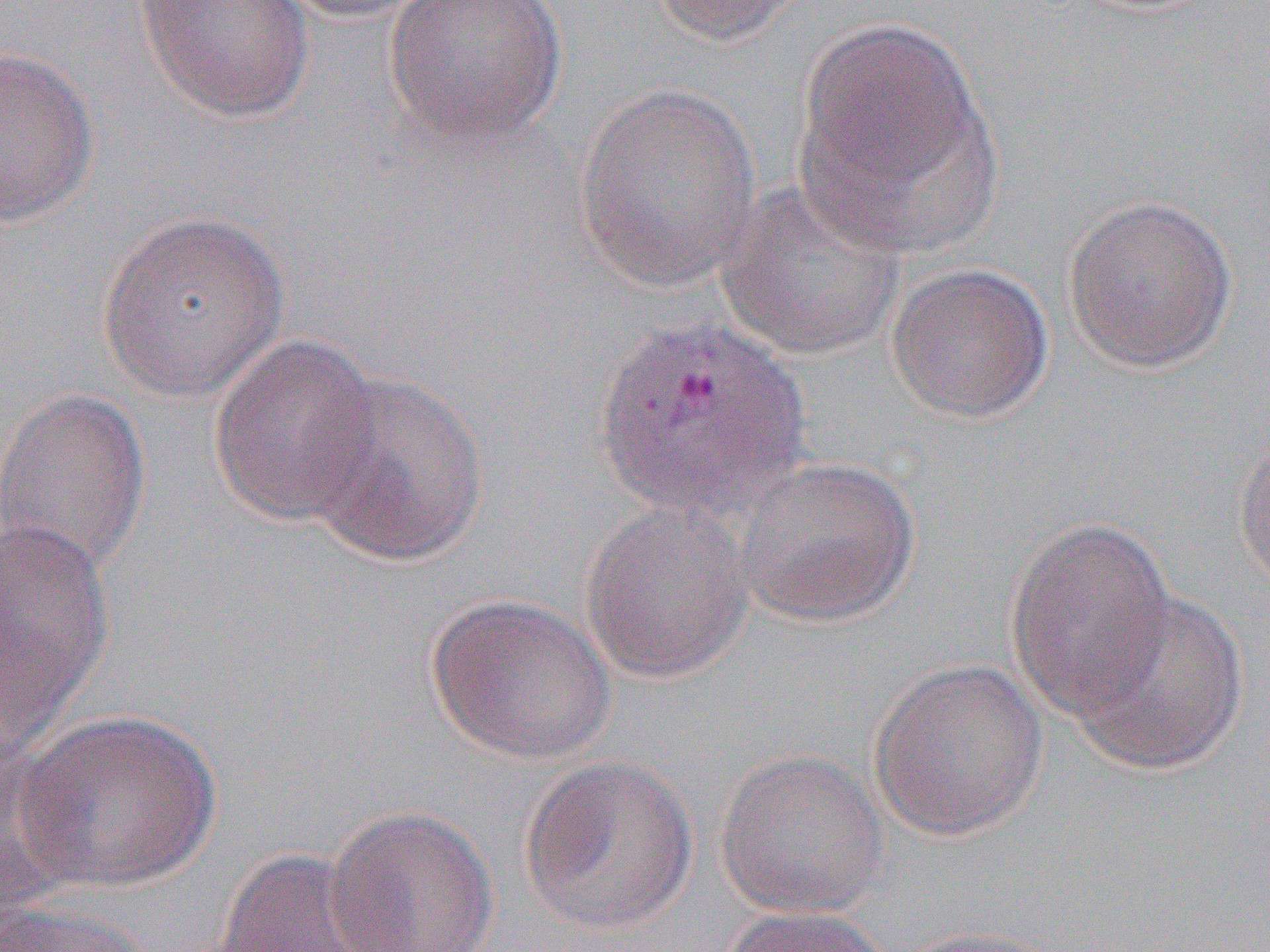
Summary:
  - Coordinate format: approximate bounding boxes as named x1/y1/x2/y2 corners in pixels
  - Uninfected red blood cell locations: (x1=133, y1=0, x2=316, y2=124), (x1=271, y1=0, x2=439, y2=24), (x1=381, y1=0, x2=568, y2=151), (x1=645, y1=0, x2=808, y2=48), (x1=792, y1=17, x2=1002, y2=254), (x1=0, y1=46, x2=100, y2=228), (x1=573, y1=81, x2=762, y2=294), (x1=714, y1=179, x2=909, y2=363), (x1=1061, y1=193, x2=1238, y2=376), (x1=96, y1=208, x2=292, y2=403), (x1=885, y1=262, x2=1055, y2=425), (x1=208, y1=332, x2=387, y2=528), (x1=300, y1=370, x2=492, y2=569), (x1=1, y1=385, x2=152, y2=579), (x1=1232, y1=423, x2=1270, y2=593), (x1=729, y1=453, x2=920, y2=628), (x1=579, y1=499, x2=755, y2=684), (x1=0, y1=513, x2=115, y2=740), (x1=1005, y1=515, x2=1177, y2=720), (x1=1064, y1=589, x2=1251, y2=777), (x1=425, y1=593, x2=618, y2=765), (x1=868, y1=657, x2=1050, y2=842), (x1=12, y1=709, x2=224, y2=894), (x1=0, y1=741, x2=81, y2=921), (x1=714, y1=748, x2=892, y2=920), (x1=518, y1=753, x2=700, y2=937), (x1=325, y1=804, x2=500, y2=952), (x1=210, y1=847, x2=402, y2=952), (x1=0, y1=900, x2=162, y2=952), (x1=716, y1=905, x2=899, y2=952), (x1=889, y1=924, x2=1070, y2=952)
  - Slide-level diagnosis: Plasmodium vivax
  - Modality: optical microscopy
  - Image size: 1270×952 pixels
  - Magnification: 1000x
  - Preparation: thin blood smear
  - Field of view: one of a larger specimen